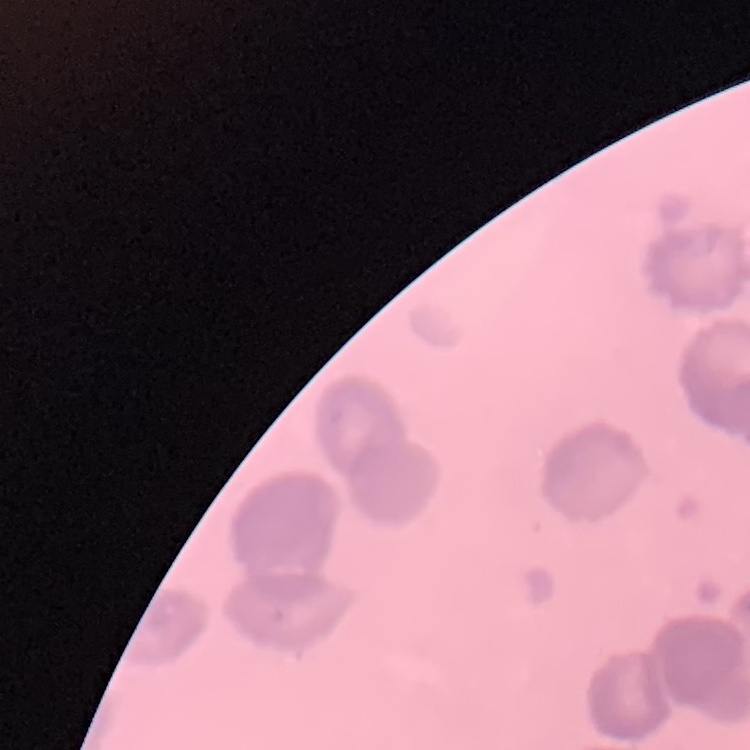 The red blood cells show rouleaux formation. Thin peripheral smear. One tile cut from a larger photomicrograph. Stained with either Field's or Giemsa.